Report the malaria status of this cell.
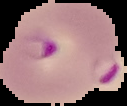
It is parasitized.

From a thin blood smear. Cell region segmented out of the field of view; the surrounding area is masked to black. Image is 127×106 pixels.